Point out each Plasmodium parasite.
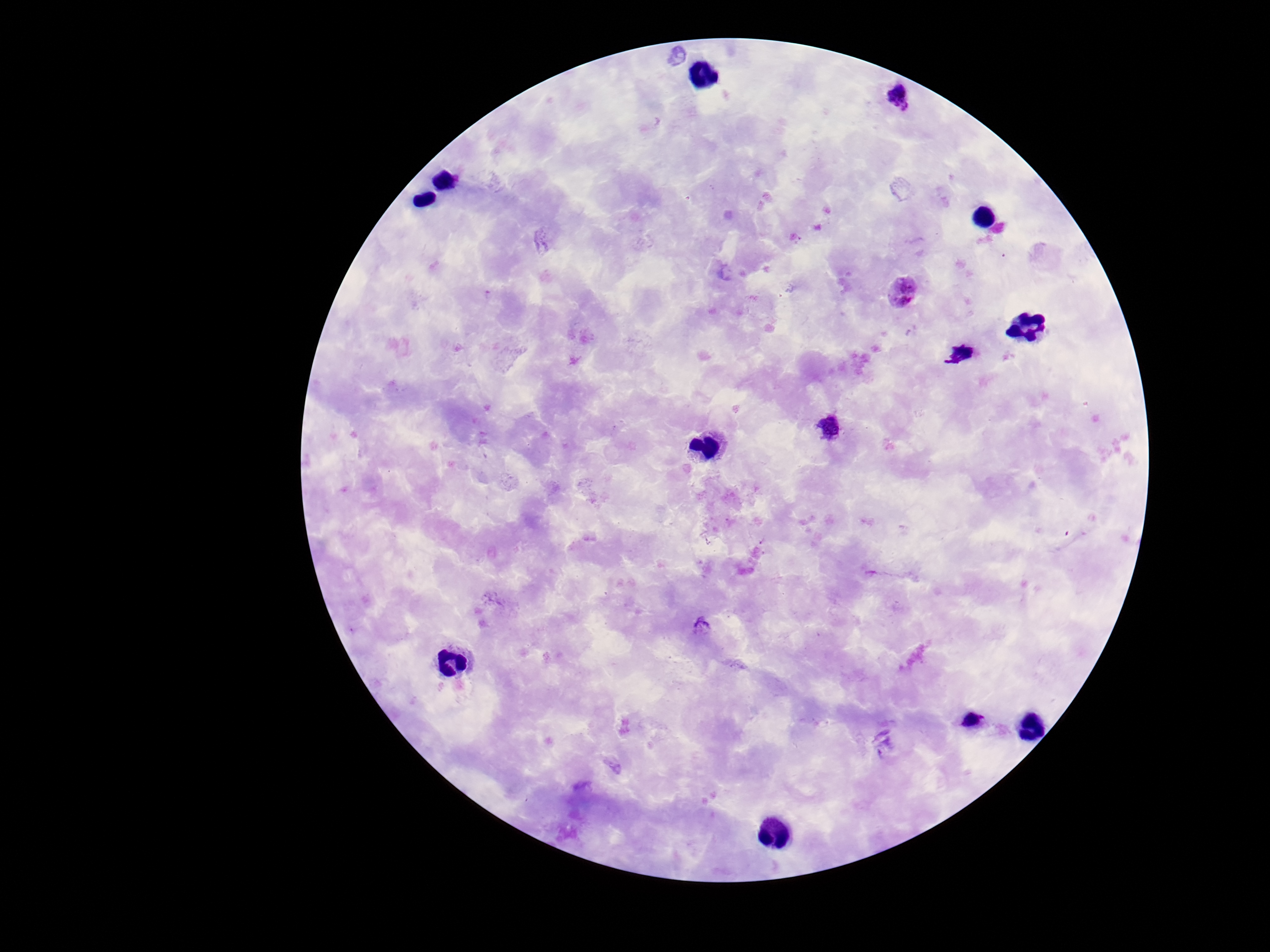

Approximate object centers, in pixels from the top-left corner.
Plasmodium parasites: (x=896, y=95), (x=902, y=292), (x=829, y=428), (x=703, y=626).

Summary:
  - Field of view: one from this slide
  - Image size: 1270×952 pixels
  - Stain: Giemsa
  - Preparation: thick blood film
  - Capture: smartphone camera through the microscope eyepiece
  - Patient malaria status: infected
  - Magnification: 100x